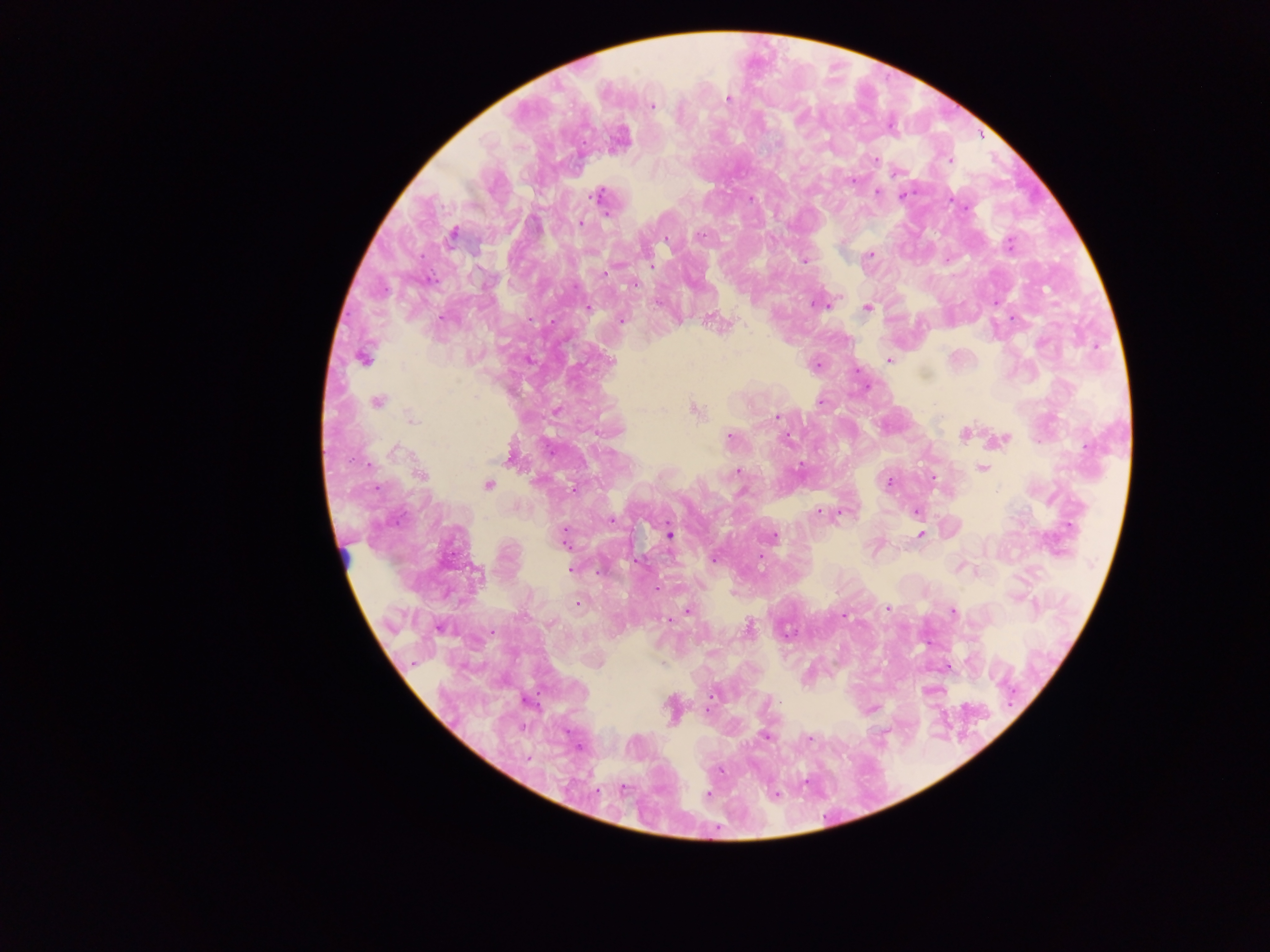
Approximate centers as (x, y) in pixels. Leukocyte locations: (344, 556). Plasmodium parasite locations: (728, 98), (652, 105), (875, 159), (949, 160), (896, 173), (852, 179), (877, 193), (902, 195), (599, 196), (750, 198), (950, 200), (581, 222), (451, 235), (1009, 244), (868, 255), (805, 260), (652, 267), (635, 284), (818, 302), (995, 302), (868, 307), (587, 309), (621, 319), (718, 323), (362, 357), (528, 359), (888, 360), (610, 361), (817, 364), (856, 371), (377, 400), (820, 401), (694, 409), (556, 411), (776, 417), (411, 419), (964, 433), (728, 438), (1002, 439), (393, 449), (511, 453), (982, 467), (737, 471), (419, 474), (933, 481), (889, 483), (488, 484), (573, 488), (820, 511), (916, 511), (830, 512), (841, 512), (611, 519), (669, 534), (920, 535), (564, 537), (771, 537), (760, 557), (714, 558), (638, 562), (571, 569), (656, 589), (888, 609), (688, 610), (952, 612), (844, 615), (668, 619), (440, 627), (748, 628), (946, 666), (713, 694), (870, 709), (707, 710), (765, 736), (708, 795). Image is 1270×952 pixels. Single field of view. Collected in Ghana. Mobile-phone photograph taken through the microscope. Thick blood film.